Classify this cell by malaria status.
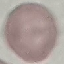

It is uninfected.

Summary:
  - Capture: smartphone camera at the microscope eyepiece
  - Stain: Giemsa
  - Preparation: thin blood smear
  - Image type: automatically extracted cell patch, resized to 64 × 64 pixels